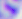

Summary:
  - Identification: Toxoplasma gondii
  - Modality: micrograph
  - Magnification: 400x